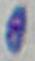
identification: Toxoplasma gondii
magnification: 1000x
modality: photomicrograph